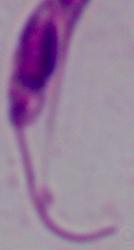

Captured at 1000x magnification. A Leishmania parasite is shown. Micrograph.